State which cell type is depicted.
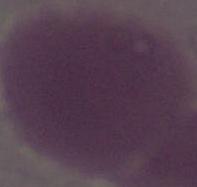
An erythrocyte.

Photomicrograph. Captured at 1000x magnification.